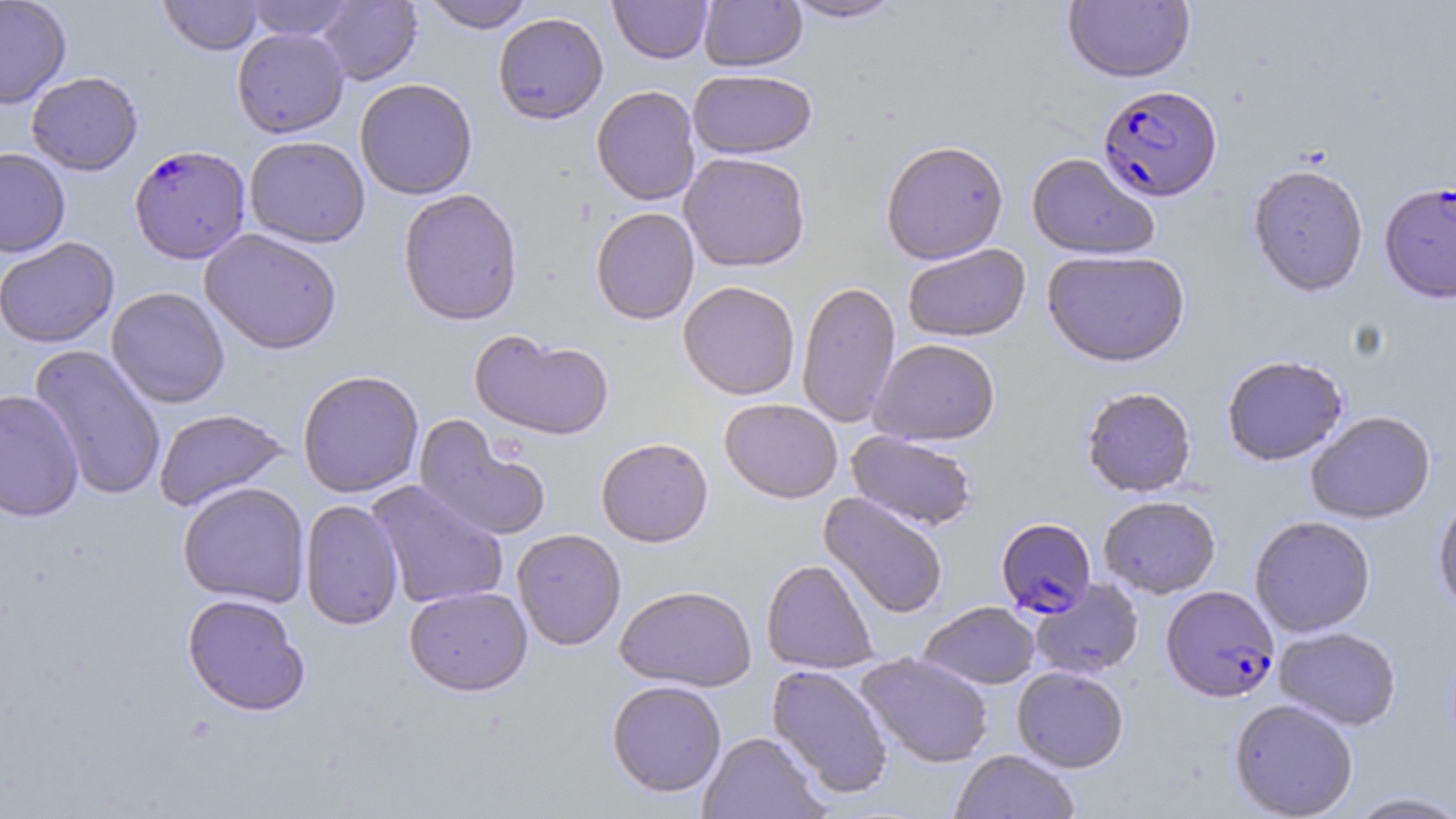

Summary:
  - Coordinate format: approximate bounding boxes as named x1/y1/x2/y2 corners in pixels
  - Plasmodium falciparum-infected red blood cell locations: (x1=1097, y1=85, x2=1223, y2=204), (x1=129, y1=144, x2=252, y2=263), (x1=1379, y1=183, x2=1456, y2=305), (x1=996, y1=518, x2=1097, y2=618), (x1=1161, y1=586, x2=1280, y2=703)
  - Uninfected red blood cell locations: (x1=0, y1=0, x2=72, y2=109), (x1=158, y1=0, x2=264, y2=56), (x1=243, y1=0, x2=359, y2=41), (x1=316, y1=0, x2=422, y2=85), (x1=419, y1=0, x2=535, y2=33), (x1=609, y1=0, x2=713, y2=64), (x1=699, y1=0, x2=807, y2=72), (x1=783, y1=0, x2=905, y2=23), (x1=1063, y1=0, x2=1195, y2=85), (x1=492, y1=12, x2=608, y2=125), (x1=231, y1=27, x2=350, y2=138), (x1=687, y1=69, x2=817, y2=159), (x1=26, y1=71, x2=143, y2=176), (x1=354, y1=78, x2=478, y2=200), (x1=591, y1=85, x2=701, y2=206), (x1=244, y1=136, x2=371, y2=248), (x1=880, y1=141, x2=1008, y2=266), (x1=0, y1=148, x2=71, y2=257), (x1=679, y1=152, x2=811, y2=272), (x1=1026, y1=153, x2=1160, y2=261), (x1=1247, y1=166, x2=1368, y2=299), (x1=397, y1=188, x2=524, y2=326), (x1=590, y1=207, x2=700, y2=325), (x1=199, y1=228, x2=343, y2=355), (x1=0, y1=237, x2=119, y2=348), (x1=903, y1=244, x2=1030, y2=344), (x1=1041, y1=251, x2=1191, y2=369), (x1=678, y1=281, x2=800, y2=400), (x1=796, y1=281, x2=901, y2=428), (x1=106, y1=287, x2=230, y2=408), (x1=469, y1=329, x2=615, y2=442), (x1=869, y1=339, x2=1000, y2=447), (x1=29, y1=344, x2=167, y2=502), (x1=1221, y1=356, x2=1349, y2=467), (x1=297, y1=369, x2=424, y2=498), (x1=1081, y1=388, x2=1197, y2=498), (x1=0, y1=389, x2=84, y2=523), (x1=719, y1=398, x2=843, y2=504), (x1=153, y1=407, x2=290, y2=512), (x1=1306, y1=411, x2=1436, y2=524), (x1=413, y1=416, x2=551, y2=542), (x1=846, y1=431, x2=978, y2=532), (x1=596, y1=437, x2=713, y2=547), (x1=366, y1=480, x2=509, y2=609), (x1=177, y1=482, x2=311, y2=607), (x1=818, y1=492, x2=949, y2=619), (x1=1098, y1=496, x2=1221, y2=599), (x1=1432, y1=496, x2=1456, y2=618), (x1=300, y1=500, x2=404, y2=631), (x1=1249, y1=516, x2=1375, y2=638), (x1=512, y1=528, x2=627, y2=650), (x1=760, y1=558, x2=880, y2=674), (x1=1031, y1=578, x2=1144, y2=680), (x1=614, y1=585, x2=757, y2=692), (x1=404, y1=586, x2=533, y2=696), (x1=181, y1=593, x2=310, y2=716), (x1=918, y1=602, x2=1041, y2=690), (x1=1273, y1=627, x2=1401, y2=731), (x1=856, y1=653, x2=994, y2=768), (x1=766, y1=664, x2=894, y2=801), (x1=1012, y1=666, x2=1129, y2=773), (x1=606, y1=680, x2=727, y2=798), (x1=1229, y1=699, x2=1358, y2=819), (x1=697, y1=732, x2=828, y2=819), (x1=951, y1=749, x2=1080, y2=819), (x1=1344, y1=790, x2=1456, y2=818)
  - Slide-level diagnosis: Plasmodium falciparum
  - Field of view: one of a larger specimen
  - Preparation: thin blood smear
  - Stain: May-Grünwald-Giemsa
  - Magnification: 1000x
  - Modality: light microscopy
  - Image size: 1456×819 pixels